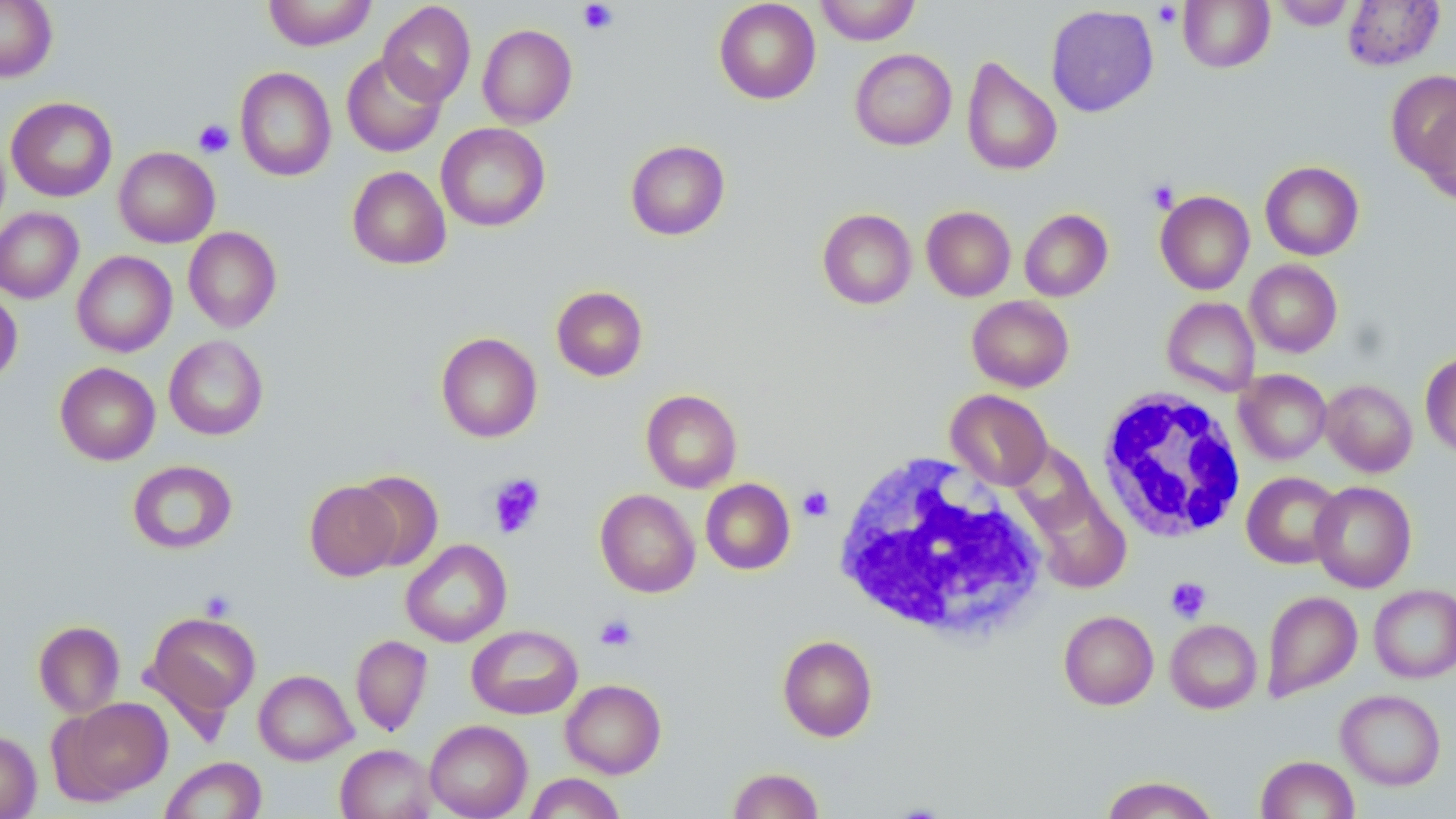
{
  "slide_level_diagnosis": "no evidence of blood parasites",
  "platelet_locations": "approximate bounding boxes as [x1, y1, x2, y2] in pixels: [578, 1, 618, 34], [1153, 3, 1183, 27], [193, 119, 234, 158], [1147, 180, 1180, 213], [487, 473, 546, 538], [798, 486, 834, 521], [1165, 577, 1211, 623], [197, 590, 237, 622], [595, 613, 638, 651]",
  "uninfected_red_blood_cell_locations": "approximate bounding boxes as [x1, y1, x2, y2] in pixels: [0, 0, 57, 82], [264, 0, 377, 50], [714, 0, 821, 104], [814, 0, 920, 45], [1178, 0, 1275, 73], [1271, 0, 1356, 30], [1343, 0, 1444, 71], [378, 2, 476, 106], [1045, 4, 1159, 117], [477, 24, 578, 128], [849, 48, 957, 151], [340, 52, 447, 157], [961, 56, 1062, 176], [235, 67, 336, 181], [1386, 70, 1456, 175], [6, 97, 117, 202], [1416, 107, 1456, 206], [436, 123, 551, 232], [625, 140, 730, 240], [114, 146, 220, 248], [1260, 161, 1364, 261], [347, 166, 451, 269], [1155, 191, 1254, 294], [921, 206, 1016, 301], [0, 207, 83, 303], [817, 208, 917, 309], [1020, 209, 1113, 301], [183, 226, 282, 332], [72, 251, 177, 357], [1245, 259, 1342, 357], [551, 285, 648, 381], [0, 288, 22, 385], [967, 295, 1074, 392], [1162, 297, 1260, 397], [436, 332, 542, 443], [164, 335, 268, 440], [1420, 351, 1456, 458], [55, 362, 160, 465], [1234, 369, 1331, 464], [1321, 379, 1417, 477], [641, 389, 742, 492], [946, 389, 1052, 490], [1008, 442, 1102, 537], [127, 460, 237, 554], [352, 470, 444, 571], [1242, 471, 1344, 569], [701, 478, 795, 575], [305, 480, 401, 581], [1310, 480, 1417, 593], [1026, 483, 1132, 594], [595, 489, 700, 597], [401, 539, 511, 647], [1369, 584, 1456, 683], [1261, 590, 1362, 701], [144, 610, 261, 723], [1059, 610, 1158, 710], [1165, 619, 1262, 713], [33, 620, 125, 717], [467, 624, 582, 719], [350, 635, 432, 737], [777, 635, 877, 742], [254, 669, 357, 765], [560, 679, 666, 778], [1336, 689, 1446, 790], [58, 697, 172, 801], [424, 719, 533, 819], [0, 729, 41, 819], [335, 744, 437, 819], [1255, 755, 1359, 819], [160, 756, 266, 818], [727, 767, 824, 819], [524, 772, 626, 819], [1100, 775, 1220, 819]",
  "field_of_view": "one of a larger specimen",
  "white_blood_cell_locations": "approximate bounding boxes as [x1, y1, x2, y2] in pixels: [1095, 387, 1249, 544], [830, 450, 1050, 643]",
  "image_size": "1456×819 pixels",
  "modality": "light microscopy",
  "stain": "May-Grünwald-Giemsa",
  "magnification": "1000x",
  "preparation": "thin blood smear"
}